Describe the morphology of the red blood cells.
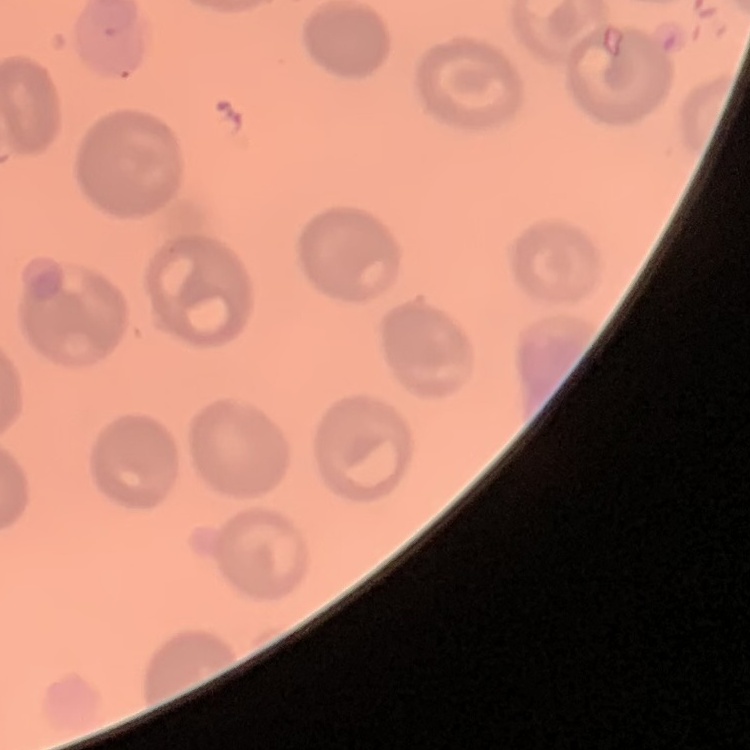
No rouleaux formation.

Summary:
  - Preparation: thin blood smear
  - Stain: Field's or Giemsa
  - Image type: square crop of a larger photomicrograph